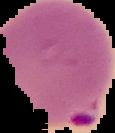

Summary:
  - Image size: 115×133 pixels
  - Result: malaria parasites detected
  - Image type: segmented cell region with the area outside set to black
  - Preparation: thin blood smear